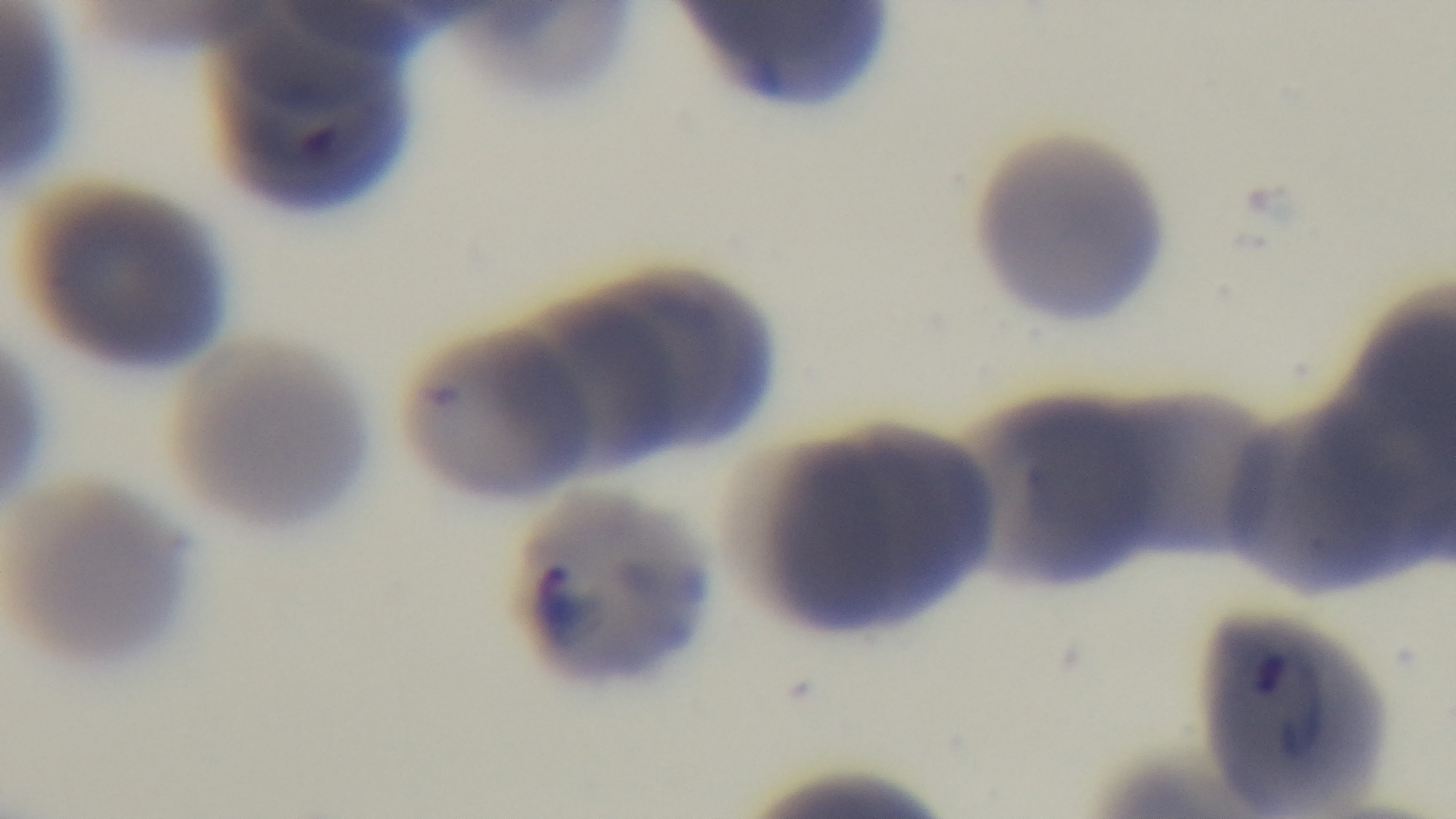 Captured with a mounted 4K digital camera. Light microscopy. Giemsa-stained. One field from the slide. Malaria status: positive. Preparation: thin blood film. Oil-immersion objective, 100x.